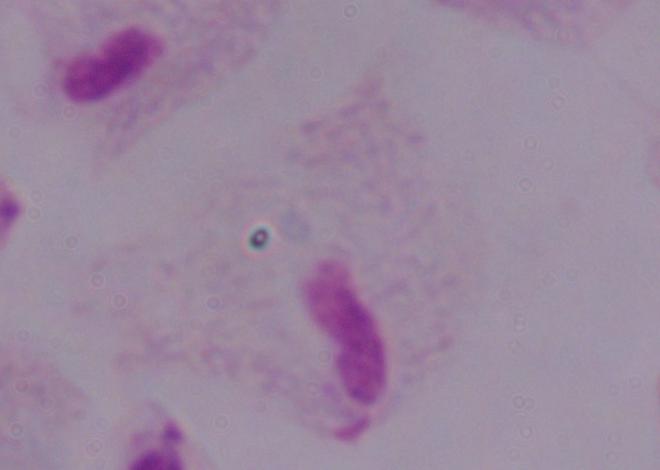
modality: photomicrograph
identification: trichomonad
magnification: 1000x